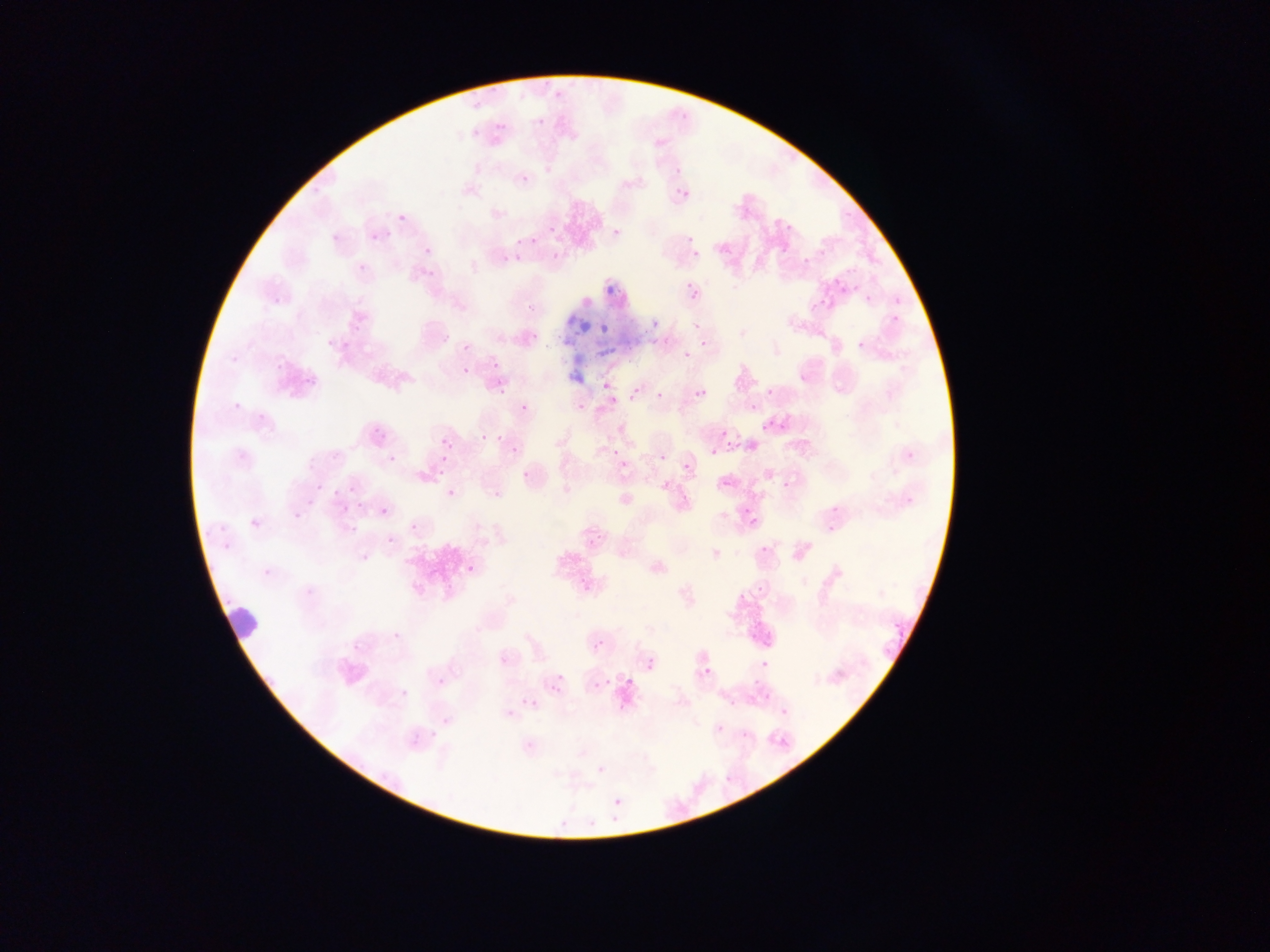
field of view = single
image size = 1270×952 pixels
country = Ghana
capture = mobile-phone photograph through a microscope
leukocyte locations = approximate bounding boxes as [left, top, right, bottom] in pixels: [215, 598, 266, 648]
preparation = thin blood smear
Plasmodium parasite locations = approximate bounding boxes as [left, top, right, bottom] in pixels: [472, 102, 481, 111], [471, 129, 480, 138], [673, 168, 681, 176], [520, 174, 530, 184], [680, 189, 690, 198], [395, 211, 407, 224], [782, 218, 798, 232], [547, 225, 556, 235], [611, 227, 622, 233], [370, 232, 380, 239], [530, 232, 540, 244], [686, 236, 695, 244], [514, 238, 523, 246], [422, 242, 434, 254], [778, 244, 794, 257], [510, 252, 524, 266], [693, 252, 701, 260], [547, 254, 557, 264], [356, 256, 368, 270], [805, 256, 816, 265], [848, 266, 857, 275], [834, 280, 850, 296], [687, 286, 701, 305], [865, 294, 874, 302], [523, 296, 544, 313], [810, 302, 818, 311], [887, 314, 904, 321], [649, 318, 658, 328], [599, 323, 609, 333], [529, 331, 543, 337], [700, 334, 711, 351], [340, 340, 349, 350], [850, 341, 862, 353], [683, 351, 691, 359], [489, 354, 500, 370], [463, 366, 470, 374], [306, 379, 316, 385], [602, 379, 612, 390], [496, 388, 506, 396], [698, 388, 708, 397], [765, 389, 774, 397], [654, 391, 663, 400], [609, 395, 619, 404], [232, 399, 243, 408], [575, 402, 588, 411], [519, 403, 529, 417], [750, 403, 759, 411], [762, 421, 776, 435], [373, 427, 382, 436], [721, 430, 729, 438], [481, 433, 490, 441], [725, 437, 735, 447], [441, 438, 451, 447], [511, 443, 522, 457], [612, 448, 619, 457], [710, 449, 718, 458], [657, 453, 667, 462], [679, 457, 691, 474], [622, 460, 632, 470], [435, 467, 448, 478], [519, 469, 534, 478], [720, 473, 730, 486], [315, 484, 324, 493], [349, 487, 358, 496], [492, 487, 502, 501], [446, 489, 455, 498], [905, 494, 915, 507], [742, 505, 749, 518], [338, 507, 346, 517], [379, 507, 388, 518], [290, 508, 301, 522], [748, 513, 761, 528], [249, 514, 257, 528], [821, 516, 842, 538], [409, 522, 419, 533], [412, 524, 424, 533], [348, 528, 355, 539], [386, 535, 395, 545], [220, 537, 226, 549], [757, 544, 768, 558], [357, 551, 371, 565], [466, 564, 475, 573], [752, 580, 766, 592], [877, 588, 889, 600], [893, 622, 906, 637], [387, 626, 399, 642], [594, 640, 604, 650], [761, 659, 771, 669], [646, 660, 655, 671], [701, 666, 711, 674], [554, 672, 565, 685], [438, 674, 446, 688], [550, 676, 566, 695], [626, 676, 634, 684], [603, 678, 612, 687], [753, 678, 763, 688], [599, 679, 610, 689], [592, 681, 606, 692], [398, 686, 409, 696], [726, 696, 736, 708], [525, 697, 539, 710], [777, 709, 783, 719], [716, 725, 724, 735], [725, 777, 733, 781], [613, 797, 622, 806]